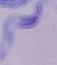
magnification: 1000x
identification: trypanosome
modality: photomicrograph